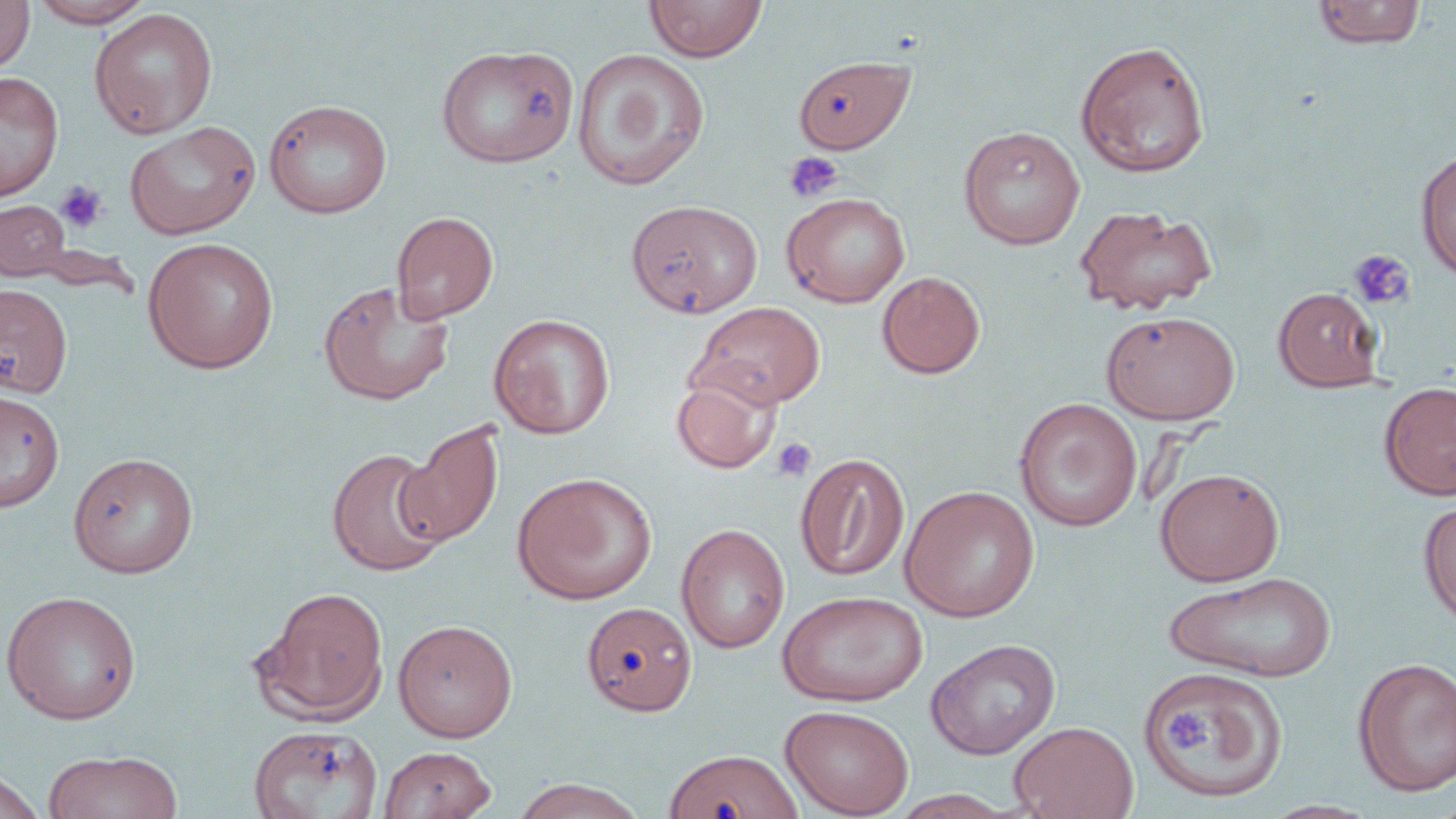
Summary:
  - Coordinate format: approximate bounding boxes as (x1, y1, x2, y2) in pixels
  - Uninfected red blood cell locations: (0, 0, 35, 72), (29, 0, 155, 28), (645, 0, 767, 62), (1311, 1, 1426, 49), (89, 8, 218, 138), (1075, 40, 1211, 178), (435, 43, 579, 168), (572, 47, 710, 191), (794, 55, 915, 153), (0, 71, 63, 201), (263, 98, 393, 219), (124, 121, 261, 239), (957, 126, 1085, 250), (1415, 147, 1456, 281), (781, 191, 910, 308), (0, 199, 72, 281), (626, 200, 763, 318), (1074, 204, 1218, 316), (391, 211, 499, 323), (142, 237, 280, 374), (876, 271, 986, 379), (317, 280, 455, 405), (0, 283, 73, 398), (1273, 287, 1383, 392), (690, 301, 827, 409), (1101, 310, 1240, 424), (488, 314, 615, 439), (671, 371, 782, 474), (1379, 381, 1456, 501), (0, 387, 64, 512), (1014, 397, 1142, 531), (398, 420, 504, 547), (327, 447, 450, 578), (67, 452, 199, 579), (794, 453, 910, 581), (1155, 468, 1284, 586), (511, 472, 657, 605), (899, 485, 1040, 622), (1418, 499, 1456, 629), (676, 523, 790, 653), (1164, 570, 1337, 682), (254, 585, 388, 724), (1, 589, 142, 725), (776, 590, 928, 707), (581, 601, 696, 716), (392, 619, 518, 743), (926, 638, 1061, 759), (1352, 657, 1456, 797), (1138, 665, 1289, 804), (780, 704, 914, 818), (1009, 721, 1138, 819), (248, 724, 382, 819), (379, 746, 497, 819), (42, 749, 182, 819), (664, 749, 802, 819), (0, 769, 44, 819), (511, 778, 646, 818)
  - Platelet locations: (783, 150, 845, 204), (55, 181, 107, 233), (1348, 249, 1416, 310), (770, 438, 817, 482), (1166, 706, 1213, 755)
  - Slide-level diagnosis: negative for blood parasites
  - Magnification: 1000x
  - Field of view: one of a larger specimen
  - Image size: 1456×819 pixels
  - Stain: May-Grünwald-Giemsa
  - Modality: optical microscopy
  - Preparation: thin blood film